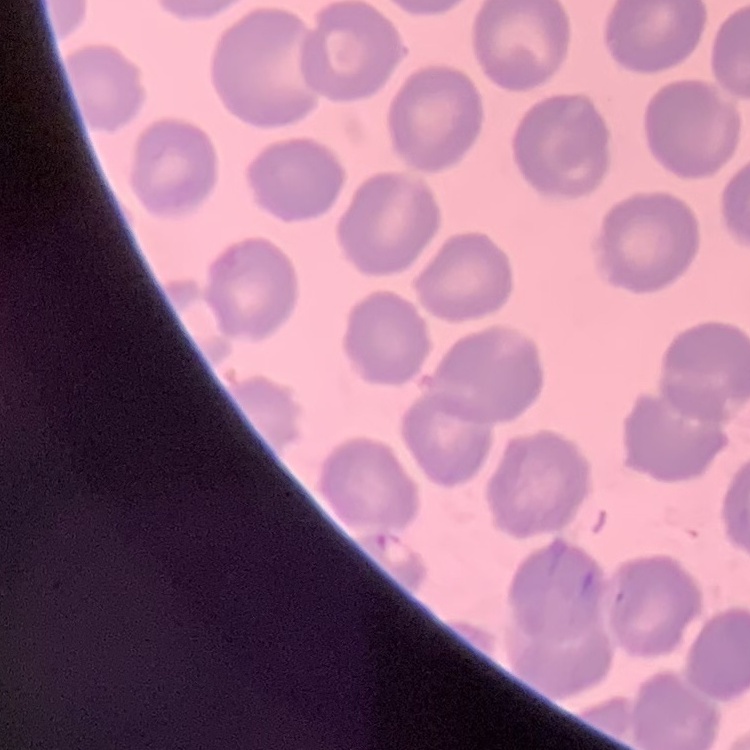
Summary:
  - Erythrocyte morphology: no rouleaux formation
  - Stain: Field's or Giemsa
  - Image type: square crop of a larger photomicrograph
  - Preparation: thin blood smear